State which cell type is depicted.
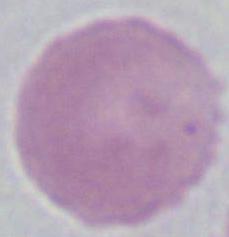
An erythrocyte.

modality = micrograph
magnification = 1000x